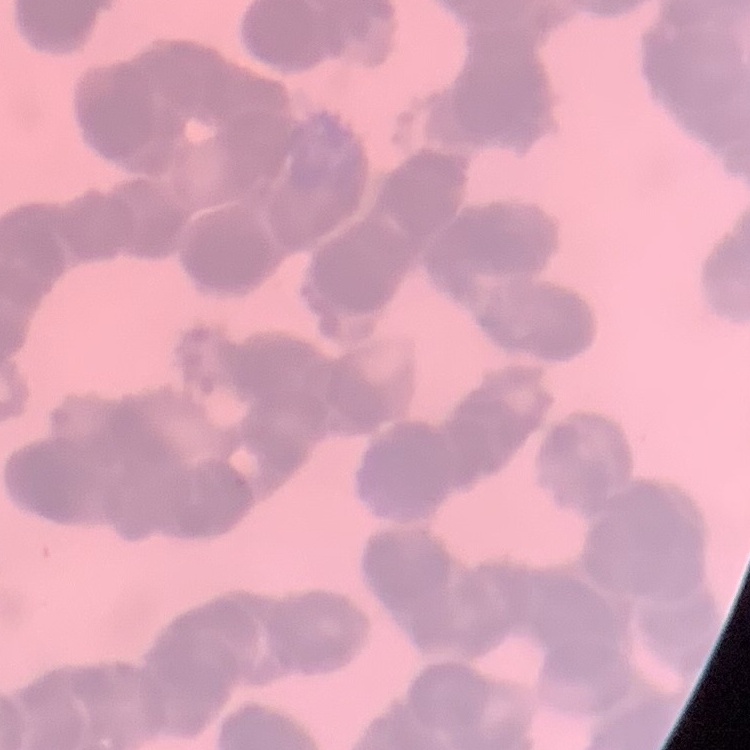
{
  "red_blood_cell_morphology": "rouleaux formation",
  "stain": "Field's or Giemsa",
  "image_type": "square crop of a larger photomicrograph",
  "preparation": "thin peripheral smear"
}